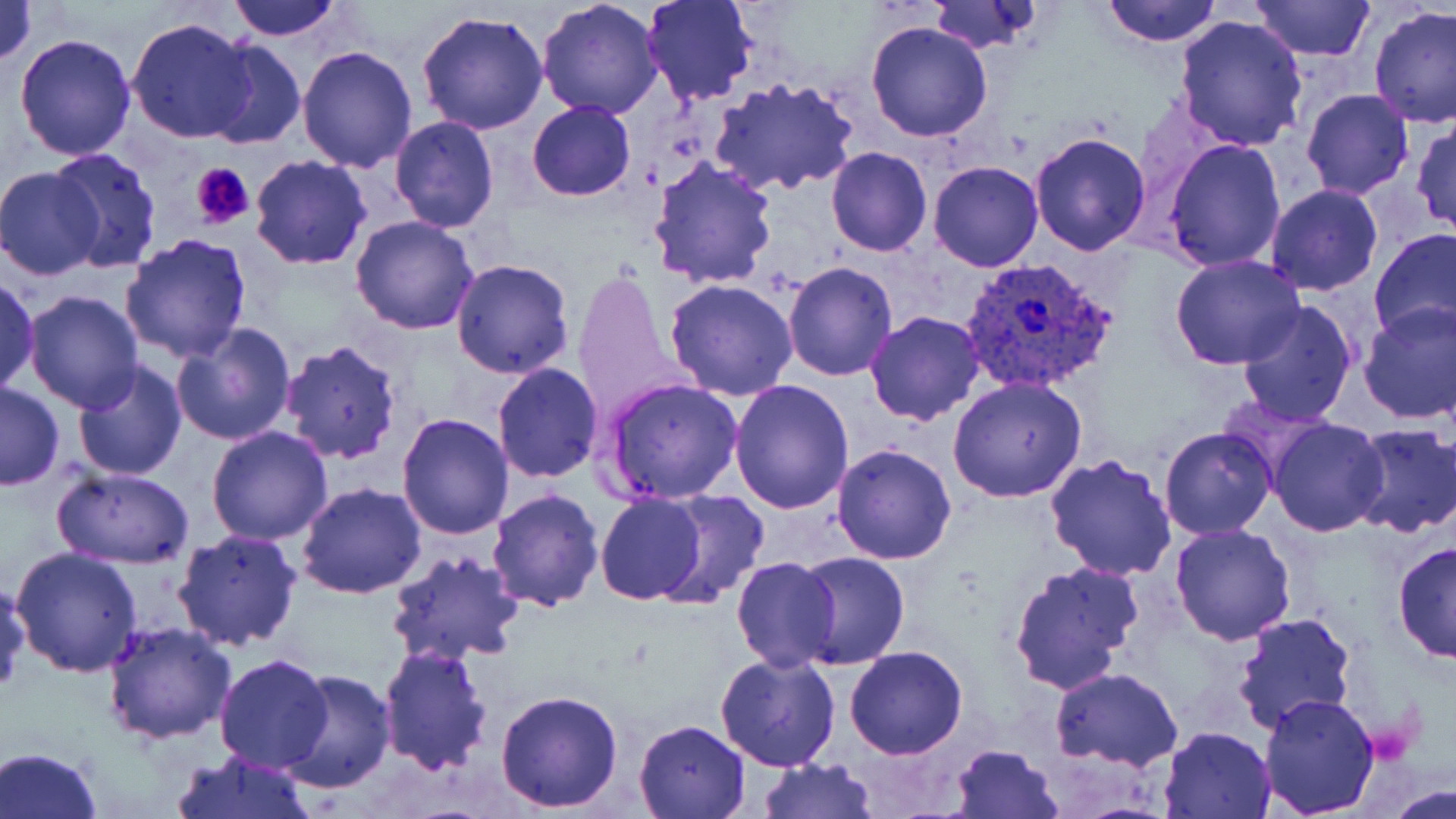 Approximate bounding boxes as named x1/y1/x2/y2 corners in pixels. Platelet locations: (x1=190, y1=163, x2=255, y2=229). Uninfected red blood cell locations: (x1=0, y1=0, x2=37, y2=66), (x1=228, y1=0, x2=346, y2=40), (x1=537, y1=0, x2=665, y2=119), (x1=642, y1=0, x2=759, y2=105), (x1=1101, y1=0, x2=1222, y2=46), (x1=928, y1=1, x2=1044, y2=55), (x1=1250, y1=1, x2=1377, y2=59), (x1=1369, y1=6, x2=1456, y2=129), (x1=417, y1=10, x2=549, y2=136), (x1=1172, y1=14, x2=1308, y2=154), (x1=126, y1=17, x2=257, y2=142), (x1=866, y1=21, x2=992, y2=142), (x1=14, y1=32, x2=137, y2=160), (x1=200, y1=39, x2=308, y2=152), (x1=296, y1=45, x2=417, y2=172), (x1=710, y1=75, x2=859, y2=194), (x1=1301, y1=88, x2=1416, y2=199), (x1=526, y1=100, x2=636, y2=201), (x1=389, y1=117, x2=498, y2=233), (x1=1410, y1=120, x2=1456, y2=236), (x1=1028, y1=132, x2=1153, y2=257), (x1=1162, y1=139, x2=1286, y2=271), (x1=826, y1=147, x2=931, y2=257), (x1=46, y1=148, x2=162, y2=272), (x1=249, y1=155, x2=372, y2=270), (x1=647, y1=157, x2=778, y2=290), (x1=929, y1=161, x2=1043, y2=273), (x1=0, y1=167, x2=105, y2=279), (x1=1263, y1=183, x2=1383, y2=295), (x1=350, y1=216, x2=478, y2=334), (x1=1368, y1=227, x2=1456, y2=345), (x1=119, y1=232, x2=253, y2=363), (x1=1170, y1=255, x2=1306, y2=370), (x1=450, y1=258, x2=575, y2=379), (x1=783, y1=263, x2=897, y2=382), (x1=572, y1=270, x2=686, y2=421), (x1=0, y1=277, x2=40, y2=394), (x1=664, y1=279, x2=798, y2=402), (x1=23, y1=289, x2=143, y2=411), (x1=1236, y1=298, x2=1360, y2=427), (x1=1357, y1=300, x2=1455, y2=423), (x1=864, y1=311, x2=984, y2=426), (x1=170, y1=321, x2=295, y2=445), (x1=280, y1=340, x2=404, y2=465), (x1=71, y1=360, x2=189, y2=480), (x1=492, y1=363, x2=604, y2=483), (x1=601, y1=377, x2=744, y2=503), (x1=948, y1=378, x2=1087, y2=503), (x1=730, y1=380, x2=855, y2=514), (x1=0, y1=381, x2=63, y2=491), (x1=397, y1=412, x2=516, y2=539), (x1=1266, y1=418, x2=1389, y2=537), (x1=1346, y1=425, x2=1456, y2=538), (x1=206, y1=426, x2=334, y2=547), (x1=1159, y1=426, x2=1277, y2=540), (x1=832, y1=442, x2=958, y2=565), (x1=1044, y1=454, x2=1177, y2=580), (x1=54, y1=467, x2=195, y2=569), (x1=296, y1=482, x2=427, y2=600), (x1=486, y1=487, x2=604, y2=611), (x1=646, y1=490, x2=771, y2=608), (x1=595, y1=494, x2=709, y2=605), (x1=1167, y1=522, x2=1296, y2=645), (x1=172, y1=529, x2=304, y2=653), (x1=1393, y1=541, x2=1456, y2=667), (x1=10, y1=548, x2=142, y2=679), (x1=387, y1=549, x2=526, y2=669), (x1=792, y1=552, x2=911, y2=669), (x1=730, y1=557, x2=841, y2=672), (x1=1008, y1=560, x2=1144, y2=694), (x1=0, y1=578, x2=29, y2=695), (x1=1230, y1=612, x2=1358, y2=739), (x1=103, y1=621, x2=236, y2=745), (x1=376, y1=643, x2=493, y2=776), (x1=844, y1=646, x2=967, y2=759), (x1=714, y1=650, x2=840, y2=772), (x1=214, y1=654, x2=334, y2=773), (x1=1049, y1=667, x2=1182, y2=770), (x1=279, y1=669, x2=395, y2=794), (x1=495, y1=689, x2=624, y2=811), (x1=1258, y1=692, x2=1380, y2=816), (x1=632, y1=719, x2=750, y2=817), (x1=1159, y1=726, x2=1276, y2=818), (x1=949, y1=743, x2=1064, y2=818), (x1=0, y1=745, x2=102, y2=819), (x1=170, y1=751, x2=318, y2=819), (x1=757, y1=758, x2=876, y2=818), (x1=1383, y1=781, x2=1456, y2=817). Plasmodium vivax-infected red blood cell locations: (x1=957, y1=256, x2=1120, y2=398). Slide-level diagnosis: Plasmodium vivax. Image is 1456×819 pixels. Thin blood film. Light microscopy. One field of a larger specimen. 1000x magnification. May-Grünwald-Giemsa-stained preparation.